Report the malaria status.
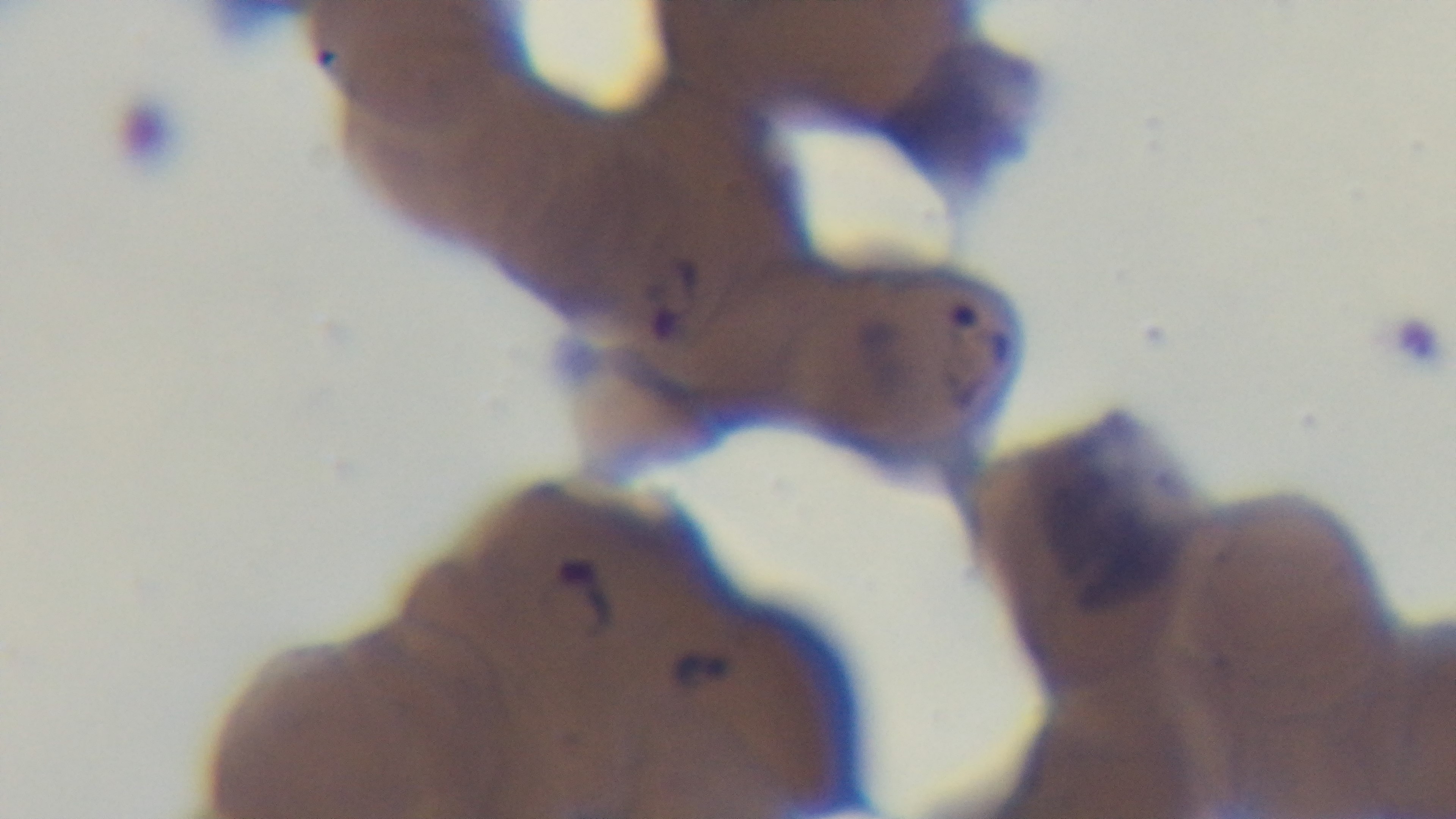
Positive.

Summary:
  - Stain: Giemsa
  - Preparation: thin
  - Objective: 100x oil immersion
  - Modality: light microscopy
  - Field of view: single
  - Capture: mounted 4K digital camera